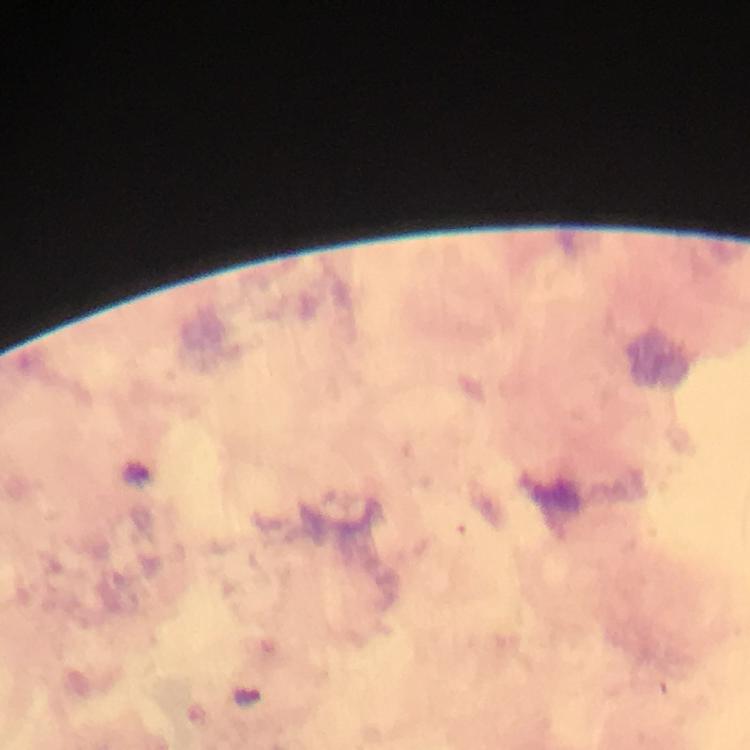
{
  "malaria_parasite_locations": "approximate centers as [x, y] in pixels: [247, 696]",
  "magnification": "100x",
  "preparation": "thick blood film",
  "context": "from a diagnostic examination for malaria",
  "cropped_from": "a single field of view",
  "image_size": "750×750 pixels",
  "capture": "smartphone photograph through a microscope",
  "immersion_oil": "used",
  "stain": "Giemsa"
}